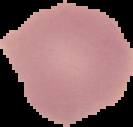
image_type: segmented cell region on a black background
image_size: 133×127 pixels
preparation: thin blood film
malaria_status: uninfected